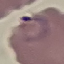

Malaria status: parasitized. Cell patch, automatically extracted from a larger field of view and resized to 64 × 64 pixels. Giemsa-stained preparation. Photographed with a smartphone camera at the microscope eyepiece. Thin blood film.